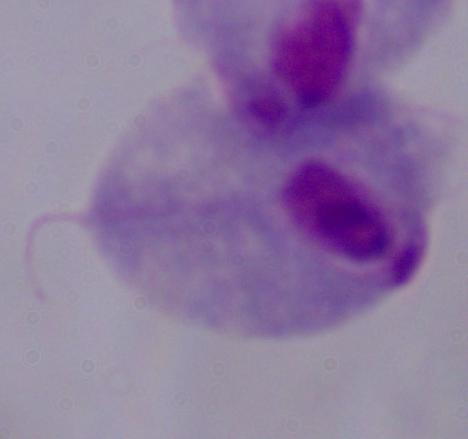
{
  "modality": "micrograph",
  "identification": "trichomonad",
  "magnification": "1000x"
}